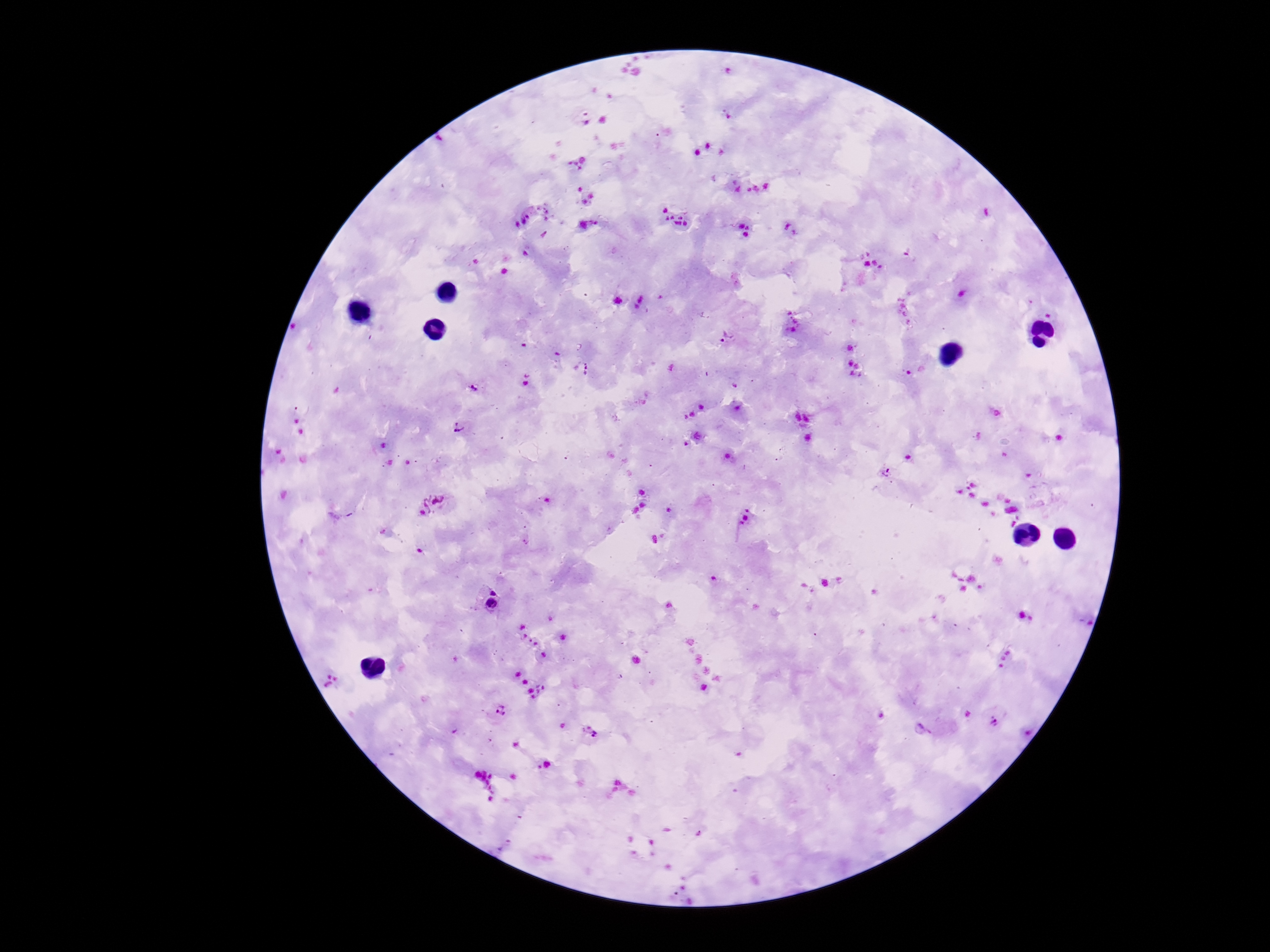

plasmodium_parasite_locations: 'approximate centers as {x, y} in pixels: {585, 118}, {525, 214}, {906, 250}, {724, 336}, {586, 369}, {527, 380}, {472, 388}, {459, 427}, {885, 473}, {432, 505}, {495, 589}, {490, 612}, {499, 713}, {995, 720}, {592, 734}'
stain: Giemsa
preparation: thick peripheral-blood smear
patient_malaria_status: positive
capture: smartphone camera through the microscope eyepiece
image_size: 1270×952 pixels
field_of_view: single
magnification: 100x